Locate every Plasmodium parasite.
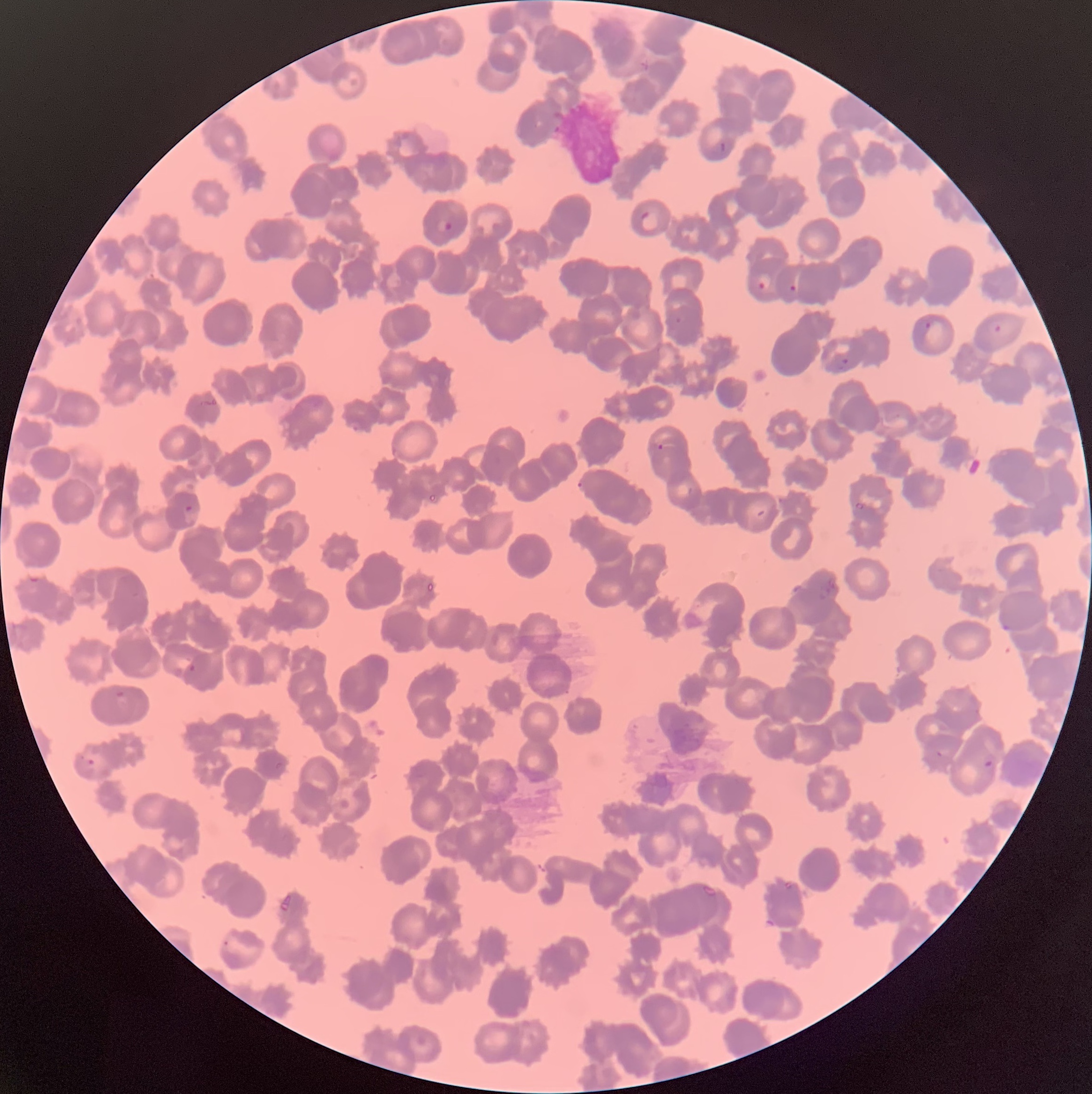
Approximate bounding boxes as [x1, y1, x2, y2] in pixels.
Plasmodium parasites: [718, 141, 727, 154], [641, 210, 661, 232], [435, 218, 453, 234], [756, 272, 772, 291], [788, 283, 797, 292], [925, 322, 932, 330], [994, 323, 1002, 332], [836, 358, 849, 370], [656, 444, 666, 451], [577, 481, 585, 488], [184, 505, 194, 513], [29, 577, 39, 584], [999, 614, 1010, 631], [187, 664, 196, 672], [115, 690, 125, 699], [936, 749, 943, 758], [982, 752, 996, 772], [87, 759, 95, 765], [281, 895, 292, 911].

modality = optical microscopy
preparation = thin blood film
red blood cell morphology = rouleaux formation
image size = 1092×1094 pixels